Name the parasite shown.
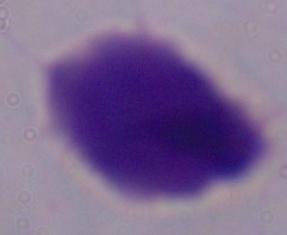

This is a trichomonad.

Summary:
  - Magnification: 1000x
  - Modality: photomicrograph